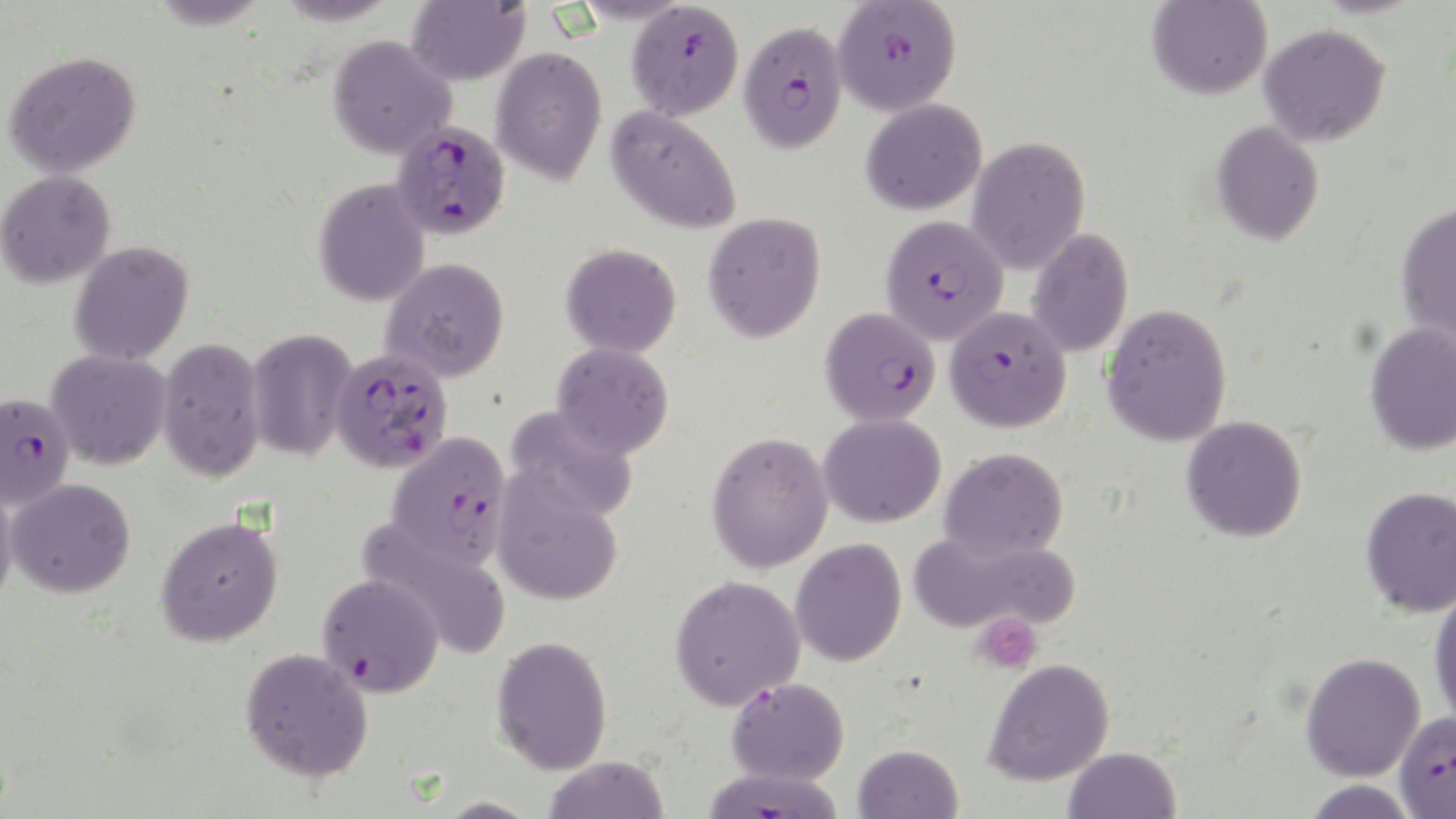

Summary:
  - Coordinate format: approximate bounding boxes as named x1/y1/x2/y2 corners in pixels
  - Uninfected red blood cell locations: (x1=276, y1=0, x2=398, y2=25), (x1=406, y1=0, x2=531, y2=86), (x1=1147, y1=1, x2=1272, y2=100), (x1=1259, y1=23, x2=1390, y2=148), (x1=328, y1=35, x2=456, y2=159), (x1=491, y1=45, x2=607, y2=184), (x1=2, y1=50, x2=141, y2=177), (x1=861, y1=97, x2=987, y2=215), (x1=607, y1=105, x2=742, y2=234), (x1=1210, y1=120, x2=1324, y2=246), (x1=966, y1=136, x2=1090, y2=274), (x1=0, y1=169, x2=116, y2=287), (x1=313, y1=178, x2=430, y2=306), (x1=1395, y1=201, x2=1456, y2=348), (x1=703, y1=211, x2=826, y2=342), (x1=1026, y1=228, x2=1134, y2=358), (x1=69, y1=241, x2=194, y2=365), (x1=561, y1=243, x2=682, y2=358), (x1=381, y1=257, x2=509, y2=381), (x1=1102, y1=303, x2=1232, y2=447), (x1=1365, y1=322, x2=1456, y2=456), (x1=247, y1=327, x2=358, y2=462), (x1=158, y1=337, x2=265, y2=482), (x1=552, y1=342, x2=675, y2=459), (x1=45, y1=349, x2=171, y2=470), (x1=505, y1=405, x2=640, y2=522), (x1=819, y1=413, x2=946, y2=527), (x1=1182, y1=416, x2=1307, y2=543), (x1=706, y1=430, x2=834, y2=573), (x1=939, y1=446, x2=1069, y2=561), (x1=492, y1=471, x2=624, y2=607), (x1=6, y1=477, x2=136, y2=598), (x1=0, y1=480, x2=18, y2=609), (x1=1360, y1=486, x2=1456, y2=617), (x1=155, y1=515, x2=284, y2=647), (x1=360, y1=519, x2=510, y2=657), (x1=908, y1=528, x2=1079, y2=636), (x1=790, y1=538, x2=907, y2=667), (x1=669, y1=573, x2=806, y2=710), (x1=1429, y1=586, x2=1456, y2=727), (x1=491, y1=635, x2=613, y2=775), (x1=239, y1=647, x2=374, y2=782), (x1=1300, y1=652, x2=1425, y2=781), (x1=983, y1=657, x2=1115, y2=786), (x1=852, y1=744, x2=963, y2=819), (x1=1063, y1=746, x2=1181, y2=819), (x1=543, y1=755, x2=669, y2=818)
  - Platelet locations: (x1=972, y1=612, x2=1043, y2=674)
  - Plasmodium falciparum-infected red blood cell locations: (x1=832, y1=0, x2=962, y2=116), (x1=626, y1=1, x2=744, y2=120), (x1=737, y1=20, x2=848, y2=155), (x1=392, y1=120, x2=510, y2=240), (x1=880, y1=214, x2=1009, y2=343), (x1=820, y1=306, x2=942, y2=427), (x1=945, y1=306, x2=1071, y2=432), (x1=330, y1=349, x2=453, y2=473), (x1=0, y1=392, x2=75, y2=510), (x1=387, y1=431, x2=513, y2=567), (x1=317, y1=573, x2=444, y2=696), (x1=726, y1=676, x2=850, y2=785), (x1=1394, y1=711, x2=1456, y2=817), (x1=701, y1=766, x2=846, y2=819)
  - Slide-level diagnosis: Plasmodium falciparum
  - Preparation: thin blood film
  - Field of view: single
  - Modality: optical microscopy
  - Image size: 1456×819 pixels
  - Magnification: 1000x
  - Stain: May-Grünwald-Giemsa